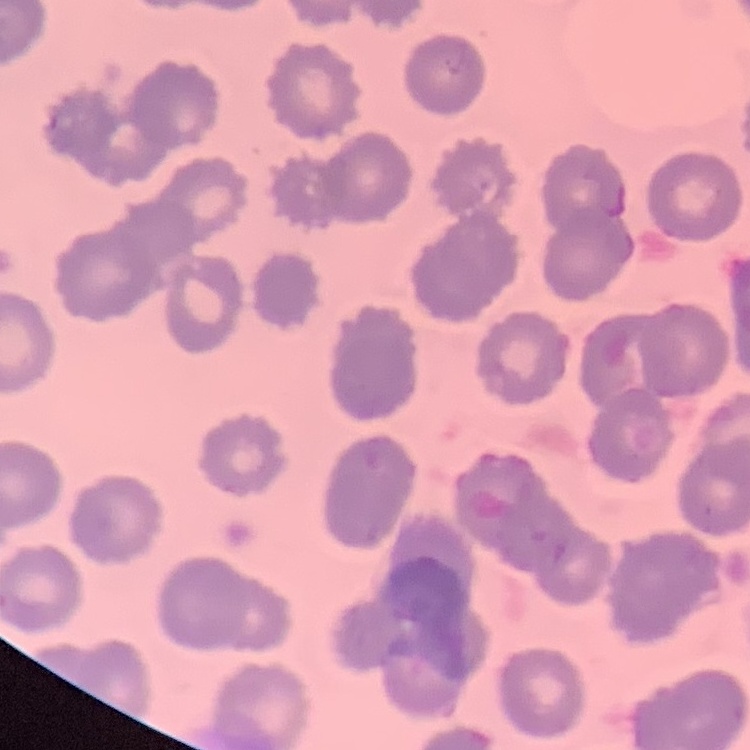

The erythrocytes exhibit no rouleaux formation. Square crop of a larger photomicrograph. Field's or Giemsa stain. Thin blood film.